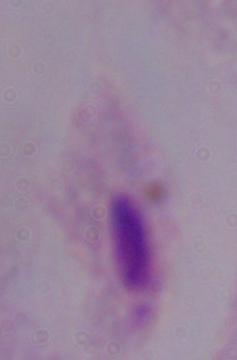

1000x magnification. Photomicrograph. A trichomonad is seen.